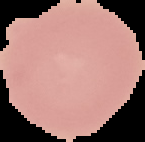

image size = 145×142 pixels
preparation = thin blood smear
image type = segmented cell region on a black background
malaria status = uninfected